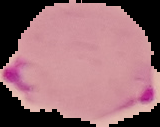 Malaria status: parasitized. From a thin blood film. Segmented cell region on a black background. Image is 160×127 pixels.